Comment on the morphology of the red blood cells.
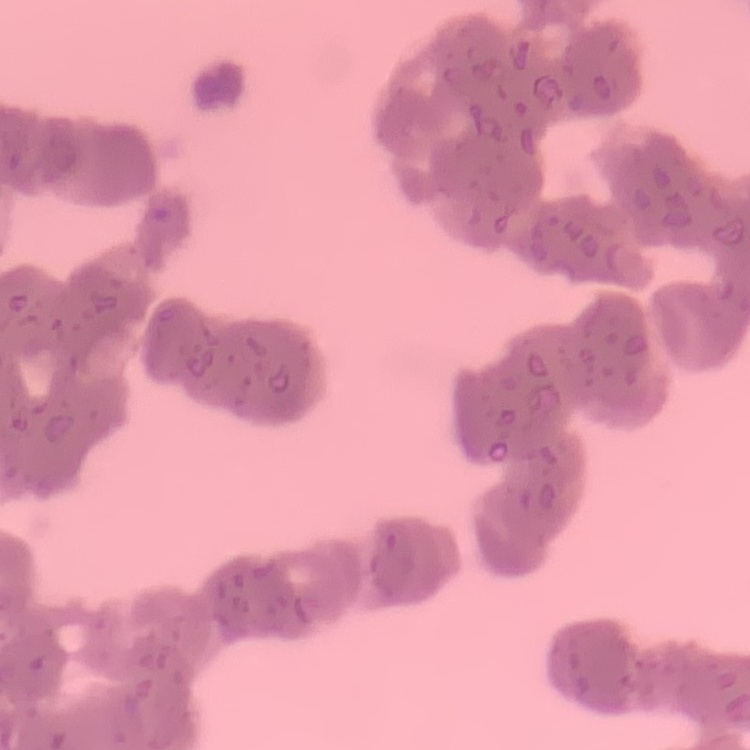
Rouleaux formation.

{
  "stain": "Field's or Giemsa",
  "preparation": "thin blood film",
  "image_type": "square crop of a larger photomicrograph"
}